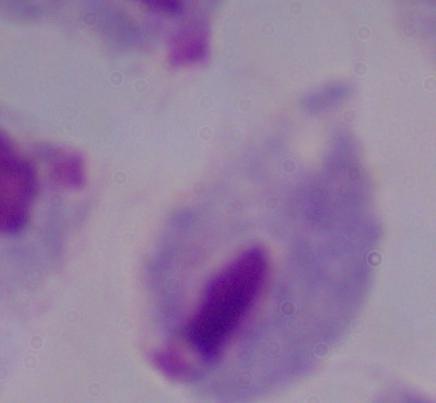

A trichomonad is seen. 1000x magnification. Micrograph.